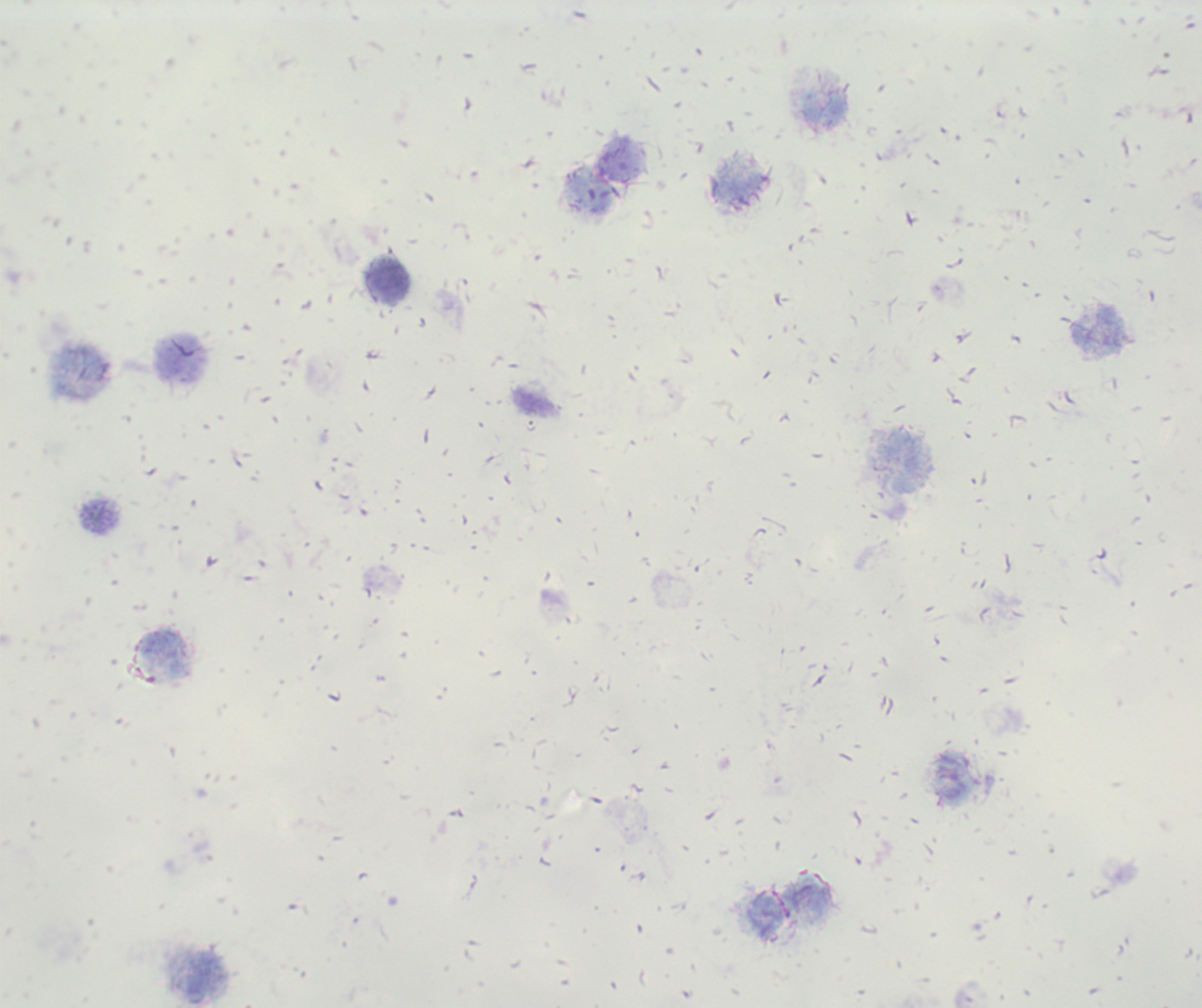

Approximate centers as [x, y] in pixels. Leukocyte locations: [824, 109], [740, 188], [389, 282], [1098, 331], [182, 359], [101, 515], [163, 655], [954, 778], [204, 978]. Result: no Plasmodium parasites detected. Background quality: poor. Previously used in an actual diagnosis. Single field of view. Romanowsky stain. Captured at 100x magnification. Thick smear of blood. Image is 1202×1008 pixels.